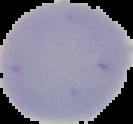
Summary:
  - Image size: 133×124 pixels
  - Image type: cell region segmented out of the field of view; surrounding area masked to black
  - Preparation: thin blood smear
  - Result: no Plasmodium parasites seen